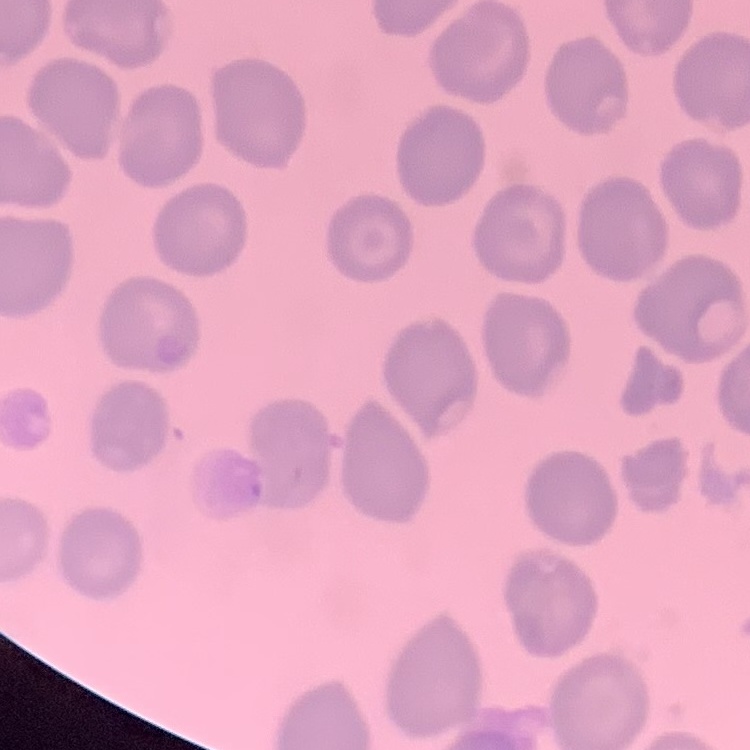

Summary:
  - Erythrocyte morphology: no rouleaux formation
  - Image type: one tile cut from a larger photomicrograph
  - Preparation: thin peripheral smear
  - Stain: Field's or Giemsa